State which parasite is depicted.
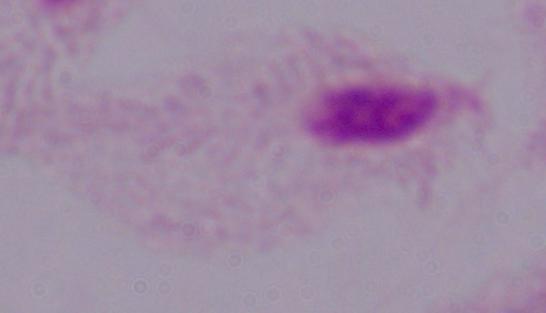
This is a trichomonad.

1000x magnification. Micrograph.